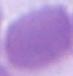 Photomicrograph. An erythrocyte is seen. 1000x magnification.